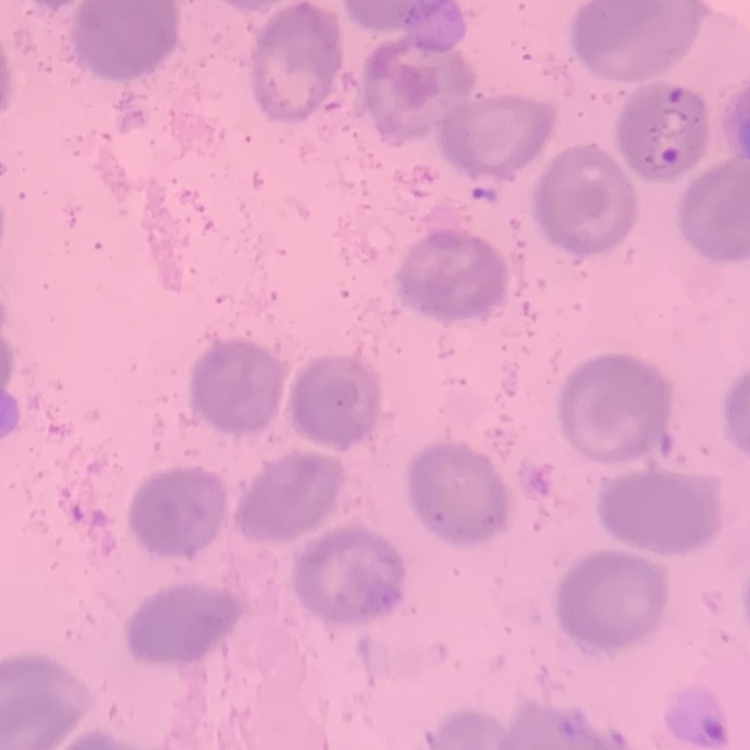

red blood cell morphology = no rouleaux formation
preparation = thin blood film
image type = one tile cut from a larger photomicrograph
stain = Field's or Giemsa